Describe the morphology of the red blood cells.
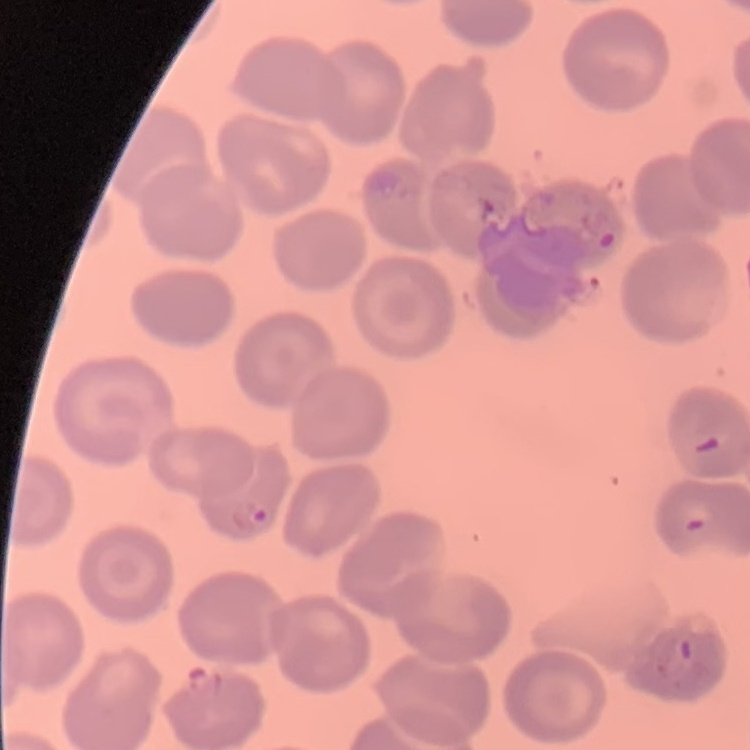
No rouleaux formation.

Stained with either Field's or Giemsa. Square crop of a larger photomicrograph. Thin peripheral smear.